Assess this cell for malaria.
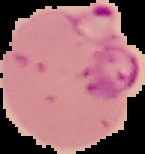
Parasitized.

preparation: thin blood film
image_size: 145×154 pixels
image_type: segmented cell region with the area outside set to black